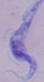

Summary:
  - Magnification: 1000x
  - Identification: trypanosome
  - Modality: photomicrograph